Point out each Plasmodium parasite.
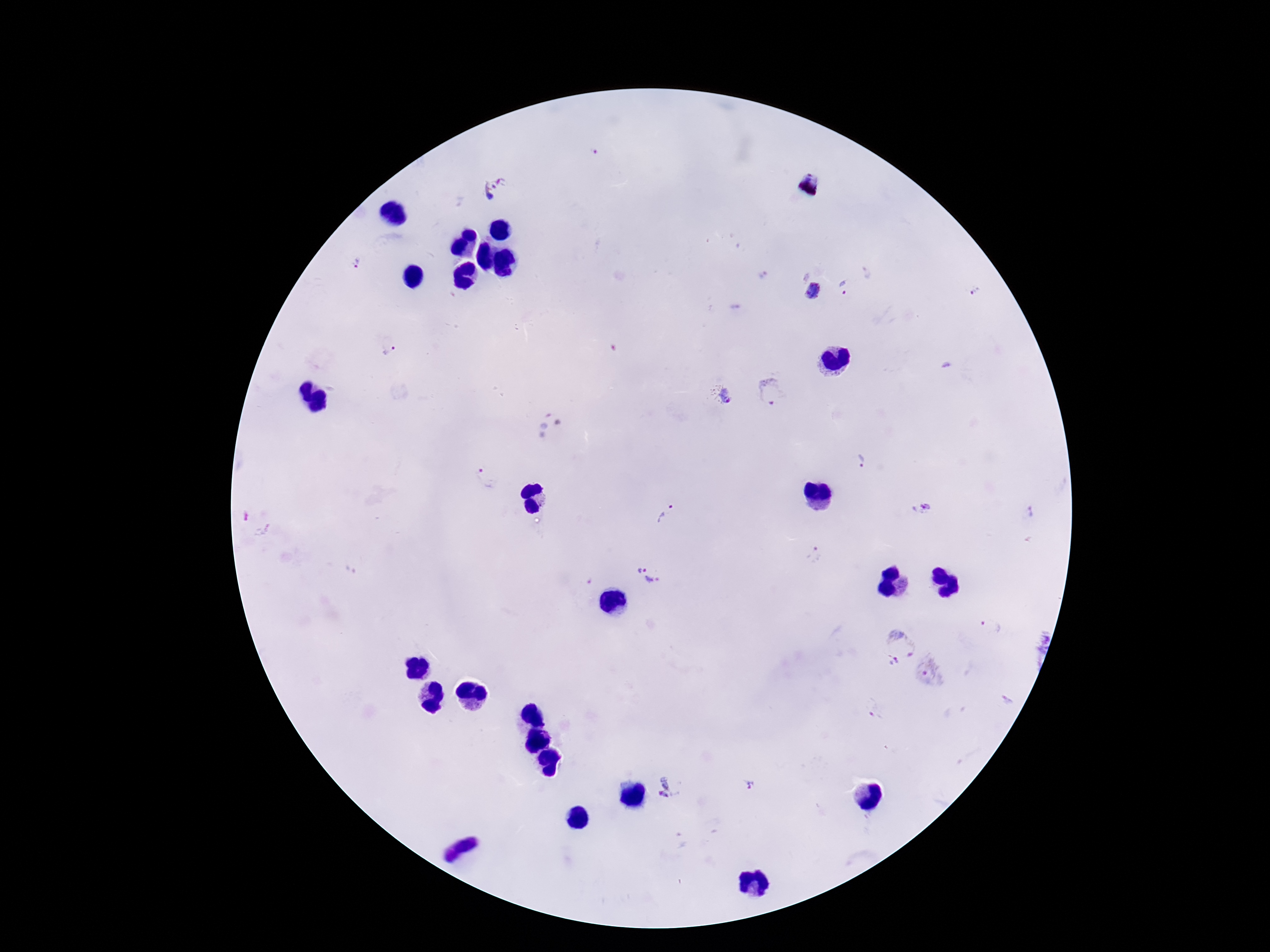
Approximate object centers, in pixels from the top-left corner.
Plasmodium parasites: (x=593, y=153), (x=494, y=188), (x=357, y=264), (x=847, y=286), (x=812, y=290), (x=977, y=290), (x=388, y=350), (x=773, y=394), (x=728, y=398), (x=864, y=463), (x=487, y=479), (x=923, y=506), (x=1031, y=511), (x=666, y=512), (x=246, y=516), (x=263, y=530), (x=815, y=555), (x=652, y=574), (x=992, y=628), (x=899, y=644), (x=894, y=662), (x=930, y=671), (x=750, y=785), (x=667, y=786).

Thick blood film. Giemsa stain. Patient malaria status: positive. 100x magnification. Single field of view. Image is 1270×952 pixels. Smartphone photograph taken through the microscope eyepiece.